Assess this cell for malaria.
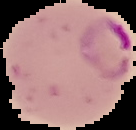
It is parasitized.

image size = 136×130 pixels
preparation = thin blood film
image type = segmented cell region with the area outside set to black